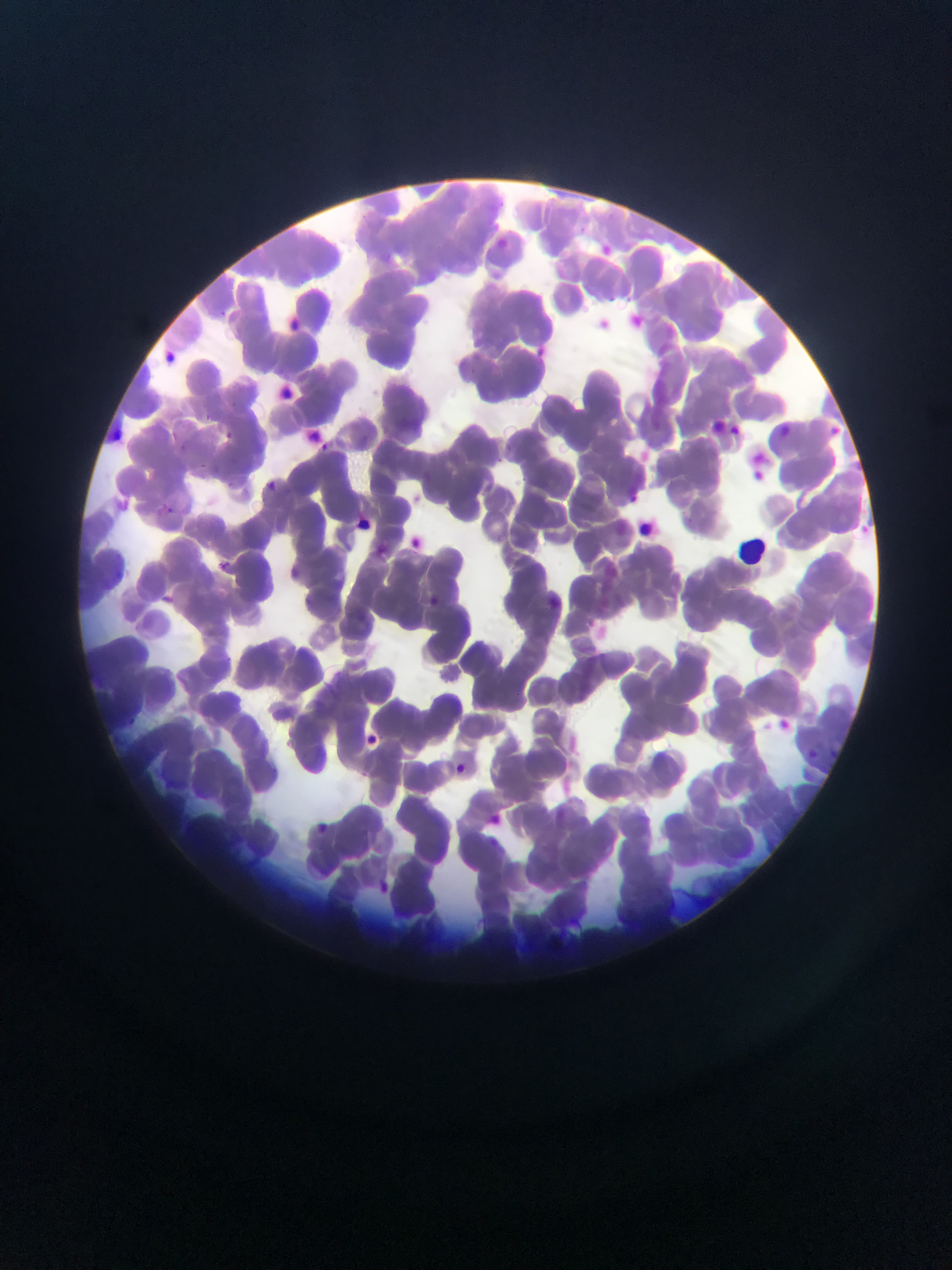 Approximate bounding boxes as (left, top, right, bottom) in pixels. Leukocyte locations: (730, 526, 770, 565). Malaria parasite locations: (574, 220, 591, 235), (203, 412, 212, 420), (225, 428, 233, 438), (316, 439, 335, 451), (180, 441, 183, 452), (193, 455, 208, 471), (221, 479, 233, 495), (268, 480, 276, 492), (114, 495, 142, 510), (159, 501, 179, 518), (376, 539, 389, 559), (217, 558, 234, 572), (127, 718, 139, 729), (827, 746, 839, 763), (804, 748, 817, 764), (454, 761, 471, 778), (317, 821, 329, 831), (490, 837, 508, 852), (381, 880, 392, 892), (652, 886, 662, 899). Mobile-phone photograph taken through the microscope. Image is 952×1270 pixels. Collected in Ghana. One field of view. Thin blood film.